Classify this cell by malaria status.
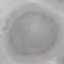
It is uninfected.

Summary:
  - Image type: cell patch, automatically extracted from a larger field of view and resized to 64 × 64 pixels
  - Stain: Giemsa
  - Preparation: thin blood film
  - Capture: smartphone through the microscope eyepiece